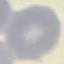

Malaria status: uninfected. Cell patch, automatically extracted from a larger field of view and resized to 64 × 64 pixels. Thin blood smear. Giemsa stain. Acquired by smartphone through the microscope eyepiece.